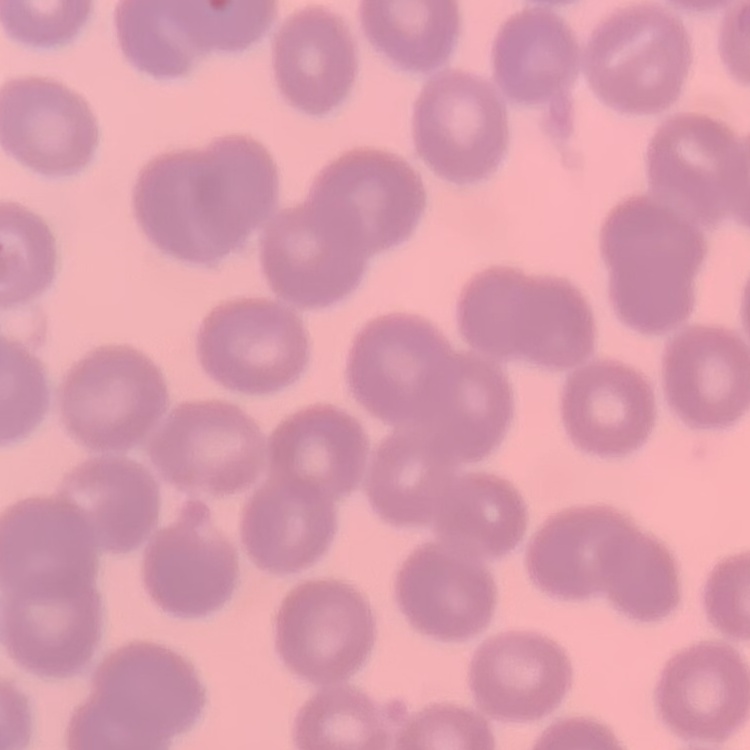
Summary:
  - Red blood cell morphology: no rouleaux formation
  - Stain: Field's or Giemsa
  - Preparation: thin blood film
  - Image type: one tile cut from a larger photomicrograph